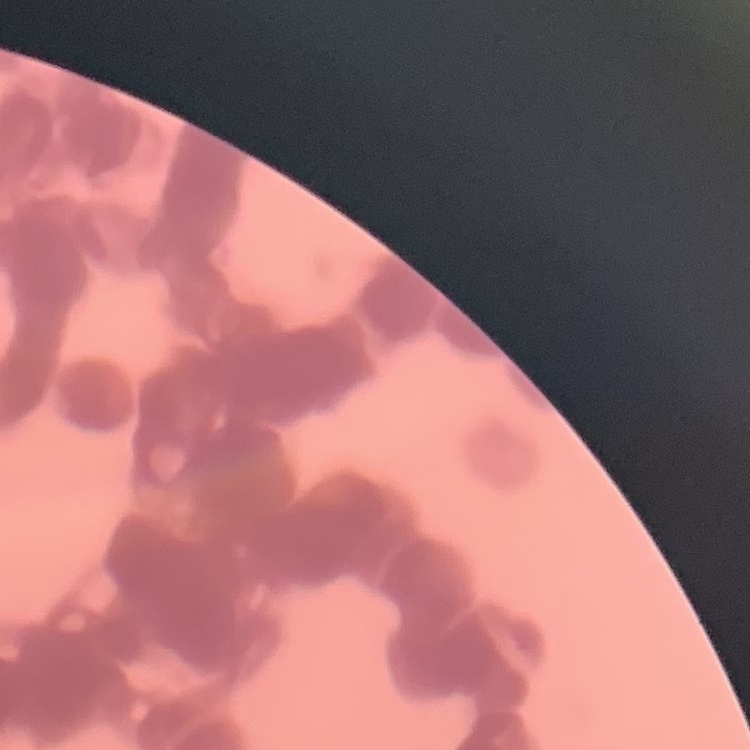 The red blood cells exhibit rouleaux formation. Thin blood film. One tile cut from a larger photomicrograph. Field's or Giemsa stain.